Locate every Plasmodium vivax-infected red blood cell.
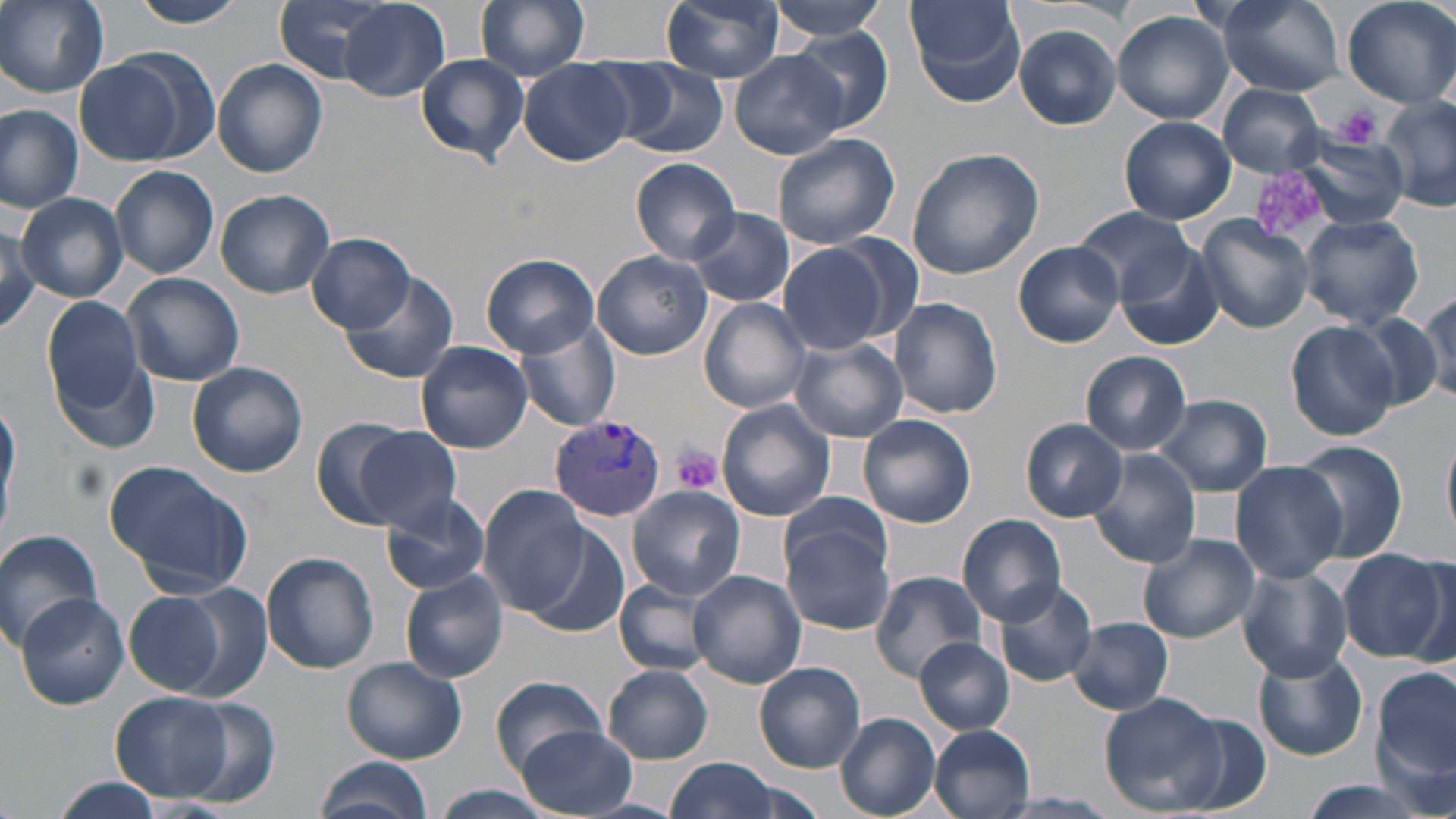

Approximate bounding boxes as (x1, y1, x2, y2) in pixels.
Plasmodium vivax-infected red blood cells: (550, 416, 667, 523).

Summary:
  - Platelet locations: (1334, 103, 1383, 148), (1249, 164, 1338, 244), (674, 446, 723, 493)
  - Uninfected red blood cell locations: (1, 0, 109, 96), (129, 0, 251, 27), (271, 0, 400, 83), (476, 0, 591, 79), (661, 0, 785, 82), (766, 0, 892, 39), (905, 0, 1026, 108), (1218, 0, 1344, 96), (1342, 0, 1456, 108), (339, 2, 449, 101), (1113, 11, 1234, 126), (1013, 23, 1123, 129), (786, 30, 895, 133), (730, 50, 850, 159), (416, 53, 529, 167), (76, 57, 189, 166), (213, 60, 328, 178), (610, 60, 729, 157), (521, 62, 631, 166), (1220, 83, 1329, 176), (1379, 97, 1456, 210), (0, 106, 82, 212), (1121, 116, 1237, 224), (771, 132, 901, 249), (1297, 134, 1410, 231), (906, 147, 1044, 280), (631, 158, 739, 264), (111, 166, 220, 279), (216, 188, 334, 298), (17, 193, 127, 303), (1072, 205, 1194, 302), (684, 206, 795, 308), (1192, 214, 1315, 333), (1298, 214, 1425, 330), (0, 220, 41, 333), (823, 230, 928, 347), (309, 233, 413, 333), (1013, 240, 1126, 346), (776, 242, 892, 356), (1116, 247, 1225, 352), (593, 250, 711, 360), (482, 253, 600, 359), (121, 272, 244, 386), (338, 272, 460, 386), (1417, 292, 1455, 403), (42, 295, 151, 423), (700, 297, 813, 414), (889, 297, 1003, 420), (1347, 310, 1447, 410), (514, 320, 621, 434), (1286, 320, 1398, 442), (790, 335, 908, 441), (414, 341, 533, 454), (50, 349, 160, 454), (1081, 350, 1191, 455), (187, 362, 308, 476), (1153, 394, 1273, 496), (0, 398, 20, 529), (715, 398, 836, 521), (858, 414, 976, 528), (309, 415, 421, 528), (1021, 417, 1128, 522), (349, 426, 463, 530), (1442, 430, 1456, 543), (1289, 441, 1412, 565), (1087, 451, 1202, 570), (104, 461, 252, 597), (1230, 461, 1347, 583), (480, 485, 590, 614), (627, 486, 744, 602), (381, 493, 490, 595), (780, 511, 898, 635), (957, 514, 1066, 624), (525, 526, 630, 638), (0, 528, 102, 648), (1138, 533, 1259, 644), (1338, 548, 1450, 662), (262, 552, 379, 676), (1399, 554, 1456, 669), (1237, 565, 1353, 682), (688, 569, 805, 688), (401, 571, 509, 684), (871, 572, 989, 681), (613, 577, 718, 676), (991, 578, 1098, 688), (154, 580, 271, 697), (124, 592, 224, 695), (16, 594, 129, 709), (1067, 617, 1174, 715), (915, 637, 1014, 735), (1253, 651, 1367, 760), (341, 656, 468, 764), (754, 659, 865, 774), (604, 666, 714, 763), (1373, 666, 1456, 783), (491, 675, 605, 775), (110, 690, 237, 802), (1099, 692, 1224, 814), (171, 698, 279, 805), (1168, 712, 1273, 813), (835, 713, 941, 819), (515, 725, 638, 818), (929, 725, 1035, 818), (312, 754, 436, 819), (666, 758, 781, 819), (50, 778, 166, 819), (1295, 779, 1436, 819), (427, 785, 557, 816), (992, 795, 1120, 817)
  - Slide-level diagnosis: Plasmodium vivax
  - Preparation: thin blood smear
  - Stain: May-Grünwald-Giemsa
  - Image size: 1456×819 pixels
  - Modality: optical microscopy
  - Field of view: single
  - Magnification: 1000x